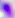
{
  "identification": "Toxoplasma gondii",
  "magnification": "400x",
  "modality": "photomicrograph"
}